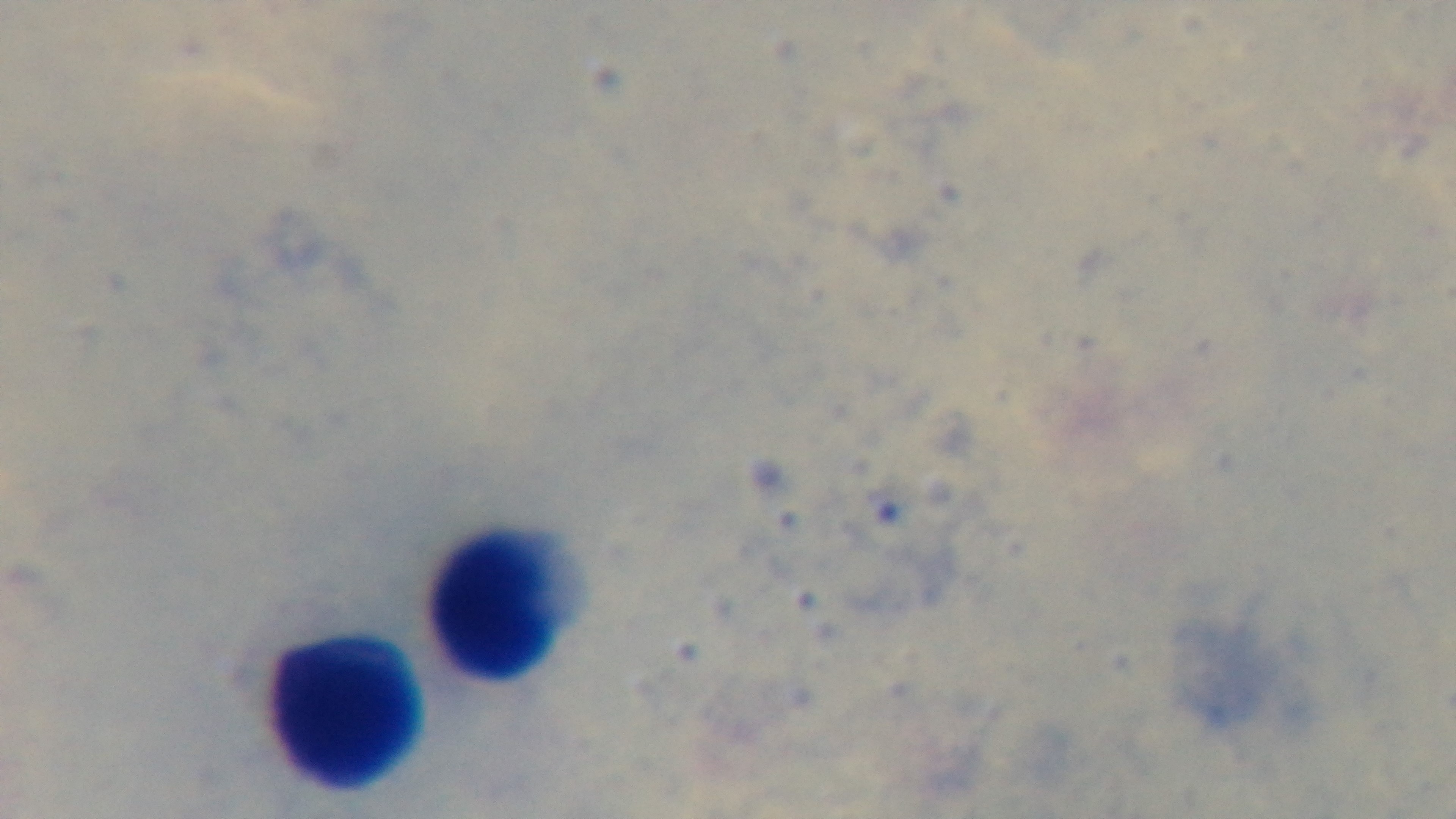

Giemsa stain. Oil-immersion objective, 100x. Single field of view. Preparation: thick smear. Mounted 4K digital camera. Photomicrograph. Malaria status: negative.